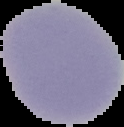 From a thin blood film. Segmented cell region on a black background. Image is 124×127 pixels. Result: negative for Plasmodium parasites.